Point out each Plasmodium parasite.
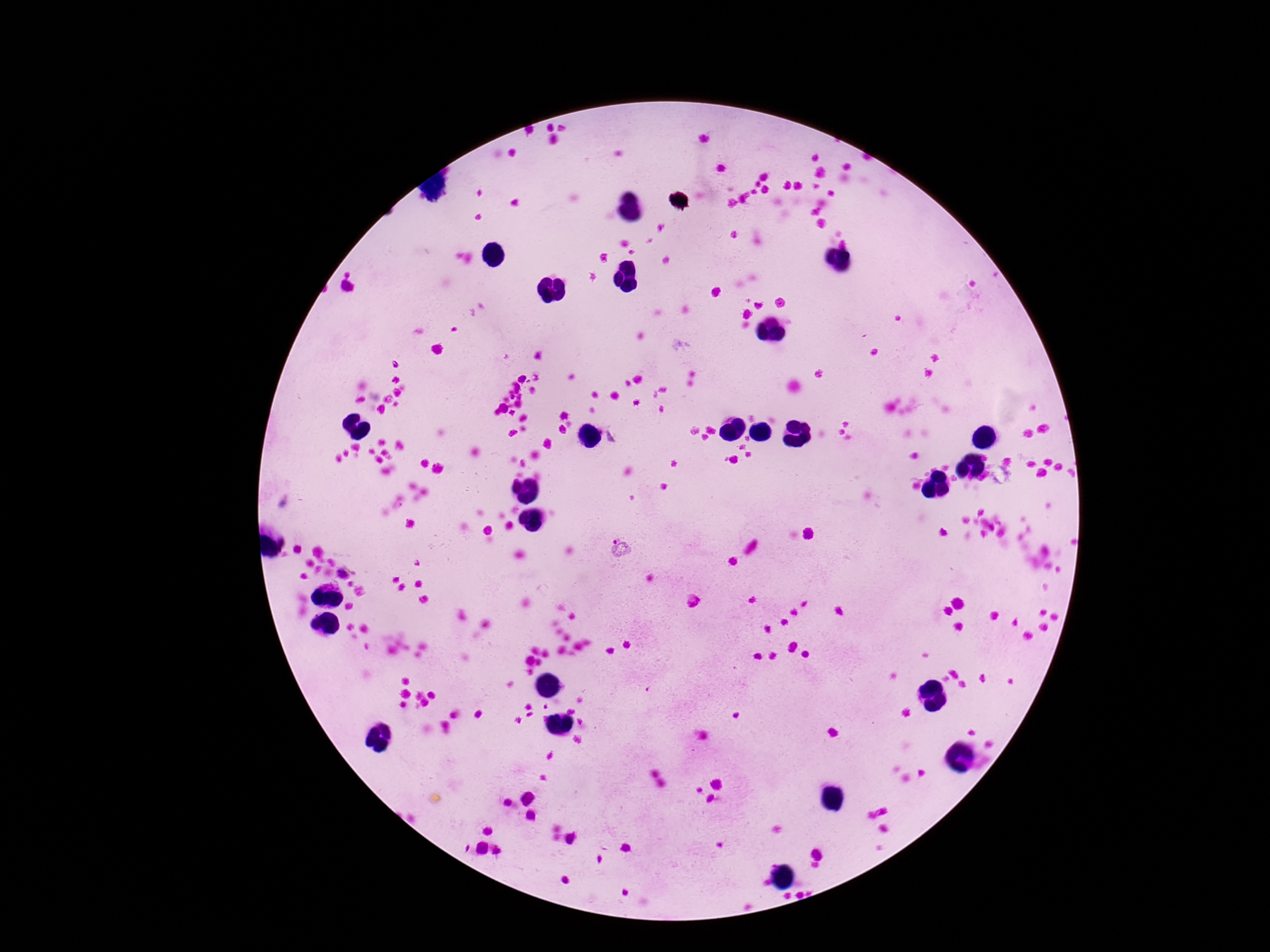
Approximate centers as {x, y} in pixels.
Plasmodium parasites: {618, 547}, {344, 575}.

Thick blood smear. One field from this slide. Photographed through the microscope eyepiece with a smartphone camera. Giemsa stain. 100x magnification. Patient malaria status: positive. Image is 1270×952 pixels.